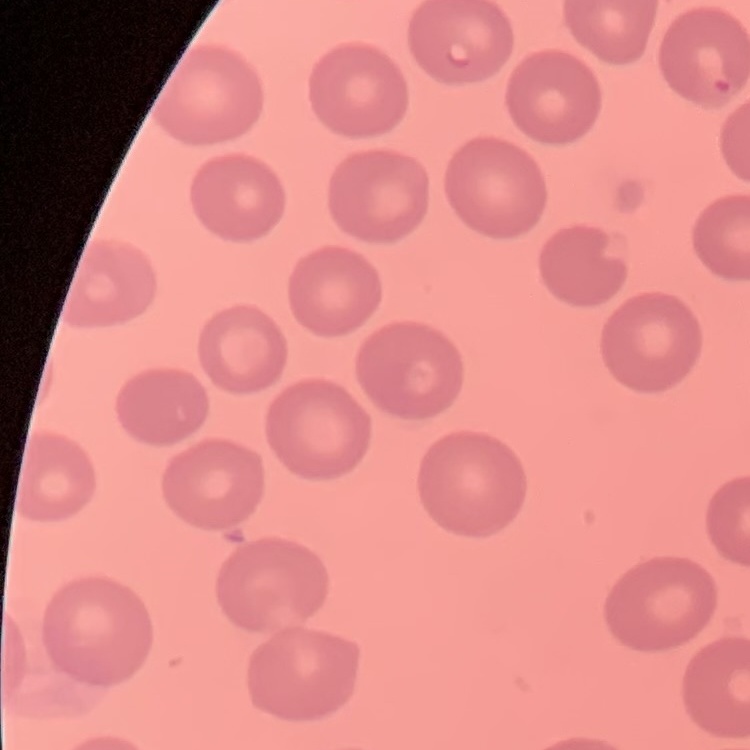

red_blood_cell_morphology: no rouleaux formation
image_type: one tile cut from a larger photomicrograph
stain: Field's or Giemsa
preparation: thin peripheral smear